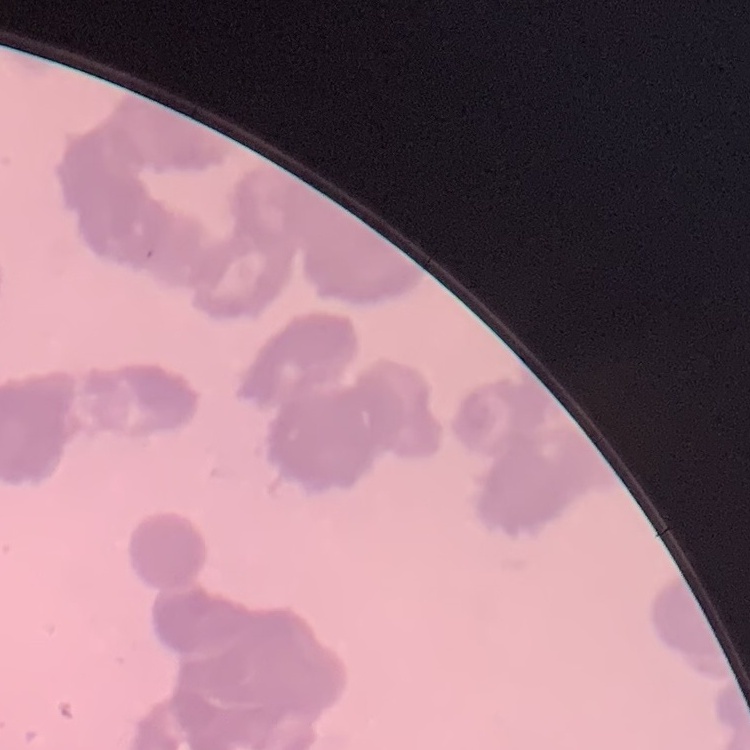
The erythrocytes show rouleaux formation. Thin peripheral smear. One tile cut from a larger photomicrograph. Field's or Giemsa stain.